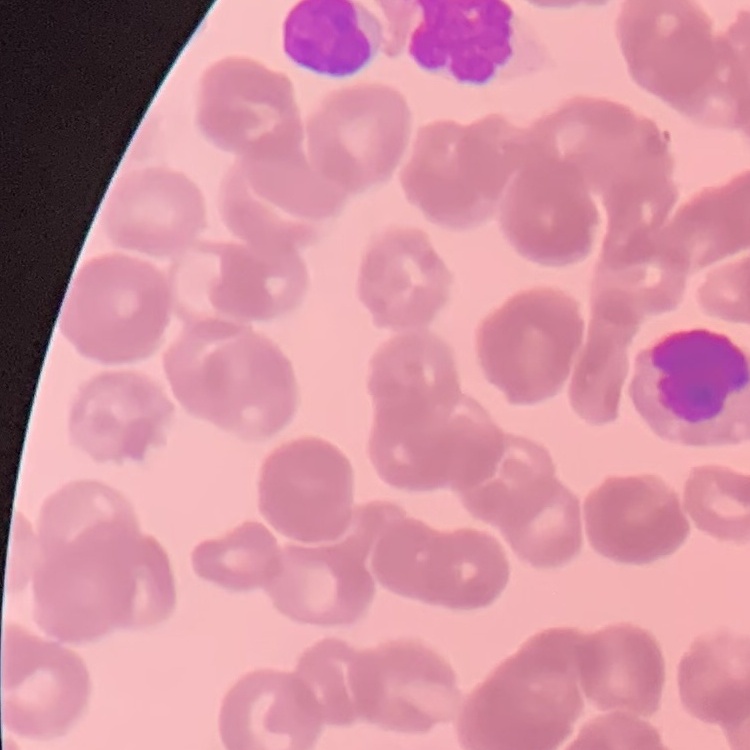

erythrocyte morphology = rouleaux formation
preparation = thin peripheral smear
image type = one tile cut from a larger photomicrograph
stain = Field's or Giemsa